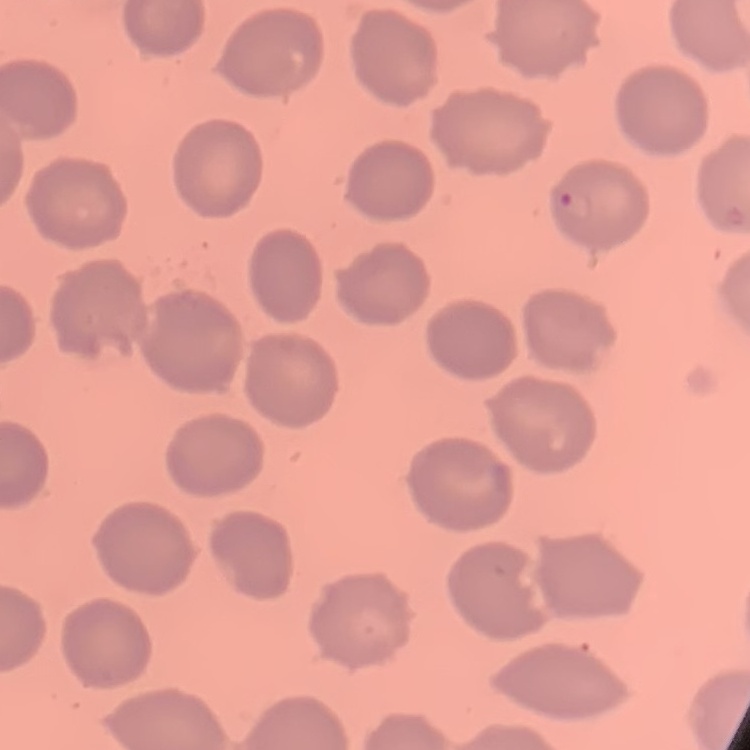
The erythrocytes show no rouleaux formation. Thin blood film. One tile cut from a larger photomicrograph. Field's or Giemsa stain.